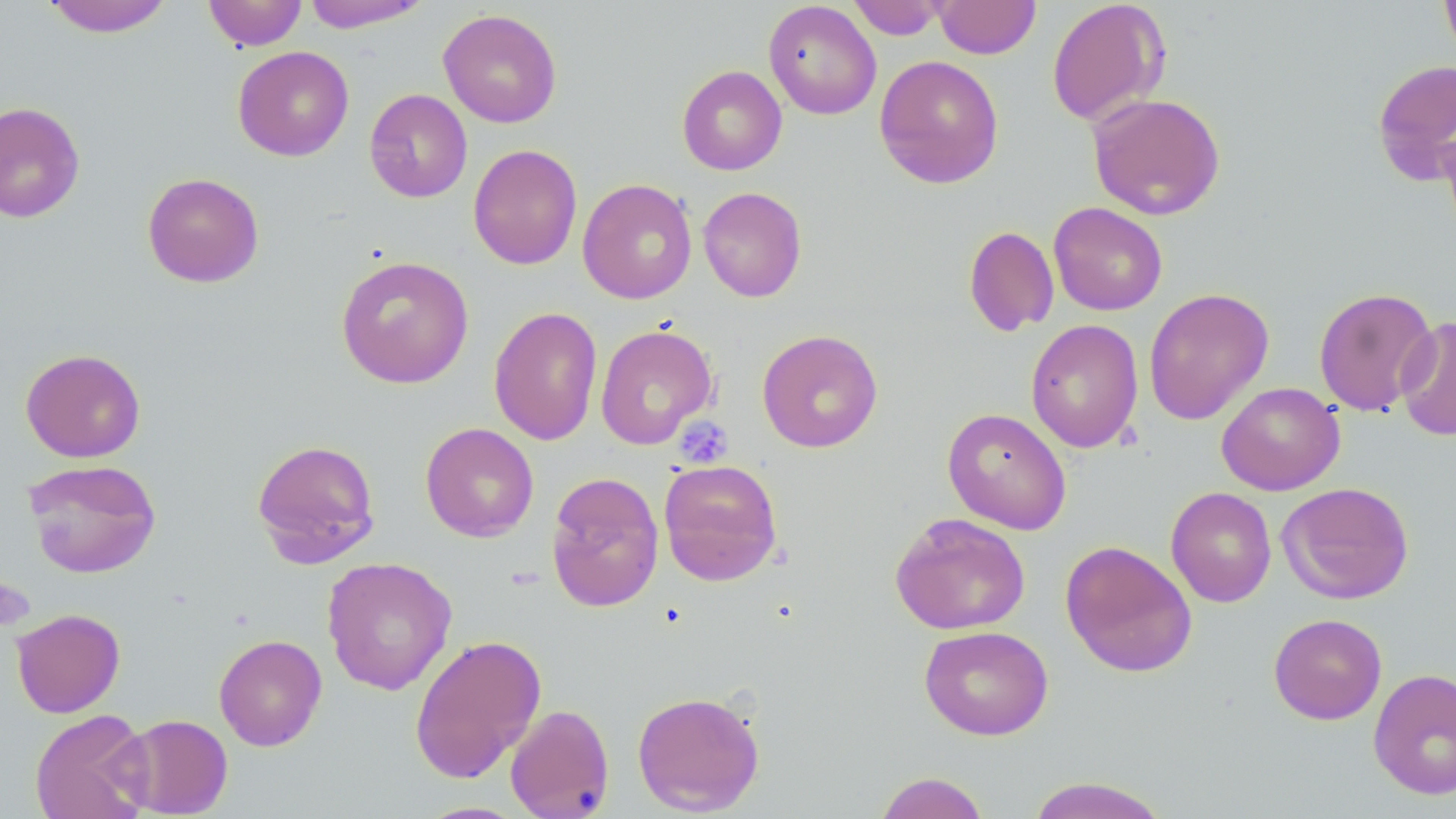
Summary:
  - Coordinate format: approximate bounding boxes as (x1,y1)-(x2,y2) corner pairs in pixels
  - Platelet locations: (674,416)-(733,470), (0,575)-(35,632)
  - Uninfected red blood cell locations: (40,0)-(176,37), (203,0)-(307,51), (848,0)-(949,40), (933,0)-(1041,59), (1046,0)-(1170,127), (1440,0)-(1456,65), (300,1)-(430,33), (763,1)-(882,120), (438,8)-(562,128), (232,46)-(354,162), (874,55)-(1004,189), (1372,58)-(1456,185), (677,65)-(787,176), (364,89)-(472,203), (1087,92)-(1226,220), (0,101)-(85,224), (1439,116)-(1456,247), (468,144)-(583,270), (142,172)-(264,288), (577,178)-(698,304), (698,187)-(807,302), (1049,202)-(1167,316), (963,226)-(1059,337), (335,255)-(474,389), (1313,286)-(1438,416), (1143,287)-(1274,426), (489,306)-(603,446), (1395,314)-(1455,442), (1026,319)-(1144,453), (595,323)-(717,450), (756,329)-(883,453), (20,348)-(146,462), (1216,382)-(1345,496), (942,407)-(1072,534), (420,422)-(539,542), (251,438)-(381,567), (23,459)-(162,579), (658,459)-(783,586), (546,471)-(665,613), (1276,481)-(1414,605), (1166,486)-(1277,607), (889,512)-(1031,635), (1060,540)-(1197,678), (321,556)-(457,696), (11,608)-(126,718), (1268,613)-(1387,725), (918,625)-(1054,741), (213,633)-(327,751), (408,633)-(546,783), (1368,667)-(1456,800), (631,690)-(765,815), (505,704)-(615,819), (29,709)-(154,819), (116,714)-(233,818), (873,771)-(991,819), (1025,776)-(1171,818)
  - Slide-level diagnosis: no evidence of blood parasites
  - Field of view: one of a larger specimen
  - Image size: 1456×819 pixels
  - Modality: light microscopy
  - Preparation: thin blood film
  - Stain: May-Grünwald-Giemsa
  - Magnification: 1000x